Give the position of every malaria parasite and every leukocyte.
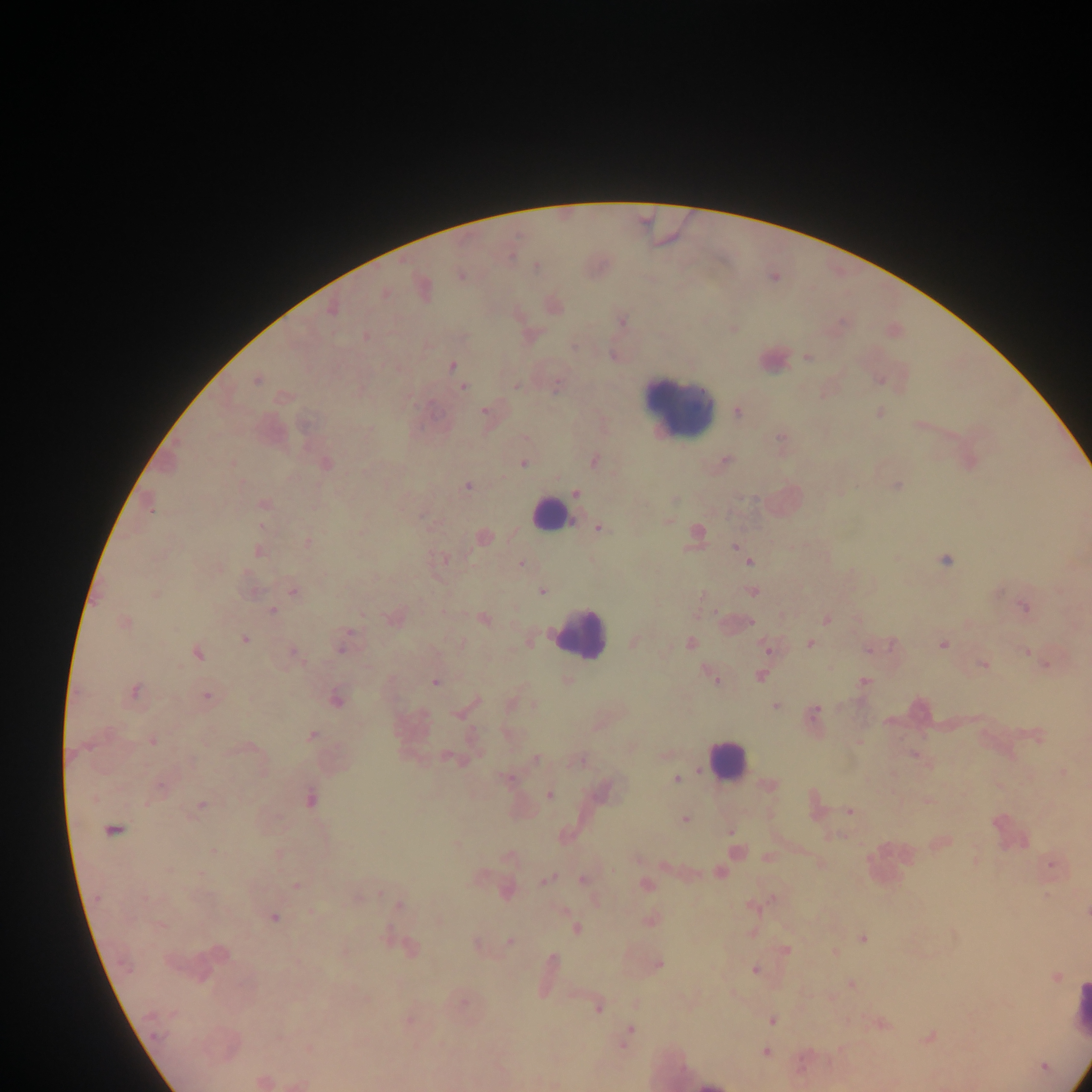
Approximate centers as (x, y) in pixels.
Malaria parasites: (536, 267), (461, 276), (385, 294), (332, 310), (622, 321), (366, 335), (574, 347), (808, 357), (453, 366), (256, 380), (556, 385), (517, 386), (463, 387), (484, 410), (738, 412), (879, 413), (782, 439), (726, 460), (594, 461), (523, 463), (232, 464), (326, 464), (897, 485), (467, 486), (575, 493), (673, 499), (264, 504), (150, 508), (261, 526), (600, 528), (697, 533), (484, 536), (307, 542), (736, 547), (258, 551), (443, 559), (945, 560), (750, 562), (521, 565), (542, 591), (293, 592), (752, 592), (155, 594), (1024, 607), (272, 610), (826, 619), (484, 620), (750, 622), (124, 623), (244, 639), (634, 642), (462, 644), (691, 644), (810, 644), (943, 645), (342, 647), (767, 648), (869, 648), (1025, 652), (198, 653), (294, 653), (982, 664), (1046, 664), (760, 676), (713, 677), (566, 682), (864, 682), (435, 683), (134, 691), (207, 697), (337, 700), (534, 704), (776, 706), (815, 712), (458, 714), (312, 735), (153, 741), (914, 755), (449, 757), (535, 758), (578, 760), (1063, 772), (507, 778), (676, 779), (769, 785), (160, 786), (549, 795), (311, 799), (927, 801), (202, 805), (849, 811), (684, 820), (112, 830), (731, 831), (834, 835), (215, 851), (510, 857), (769, 858), (637, 859), (820, 864), (1051, 865), (169, 869), (719, 873), (201, 874), (546, 880), (583, 880), (647, 885), (296, 886), (379, 893), (1046, 895), (399, 905), (753, 906), (311, 912), (1087, 913), (274, 917), (651, 920), (160, 925), (576, 930), (386, 936), (863, 938), (510, 941), (411, 950), (786, 950), (836, 953), (553, 959), (658, 963), (755, 970), (1056, 976), (851, 984), (636, 1003), (597, 1008), (773, 1021), (881, 1024), (630, 1032), (930, 1038), (625, 1043), (766, 1051), (1044, 1066), (261, 1081), (708, 1085).
Leukocytes: (678, 408), (548, 514), (579, 634), (726, 762), (1078, 1006).

Collected in Ghana. Mobile-phone photograph taken through the microscope. Thick blood smear. Single field of view. Image is 1092×1092 pixels.